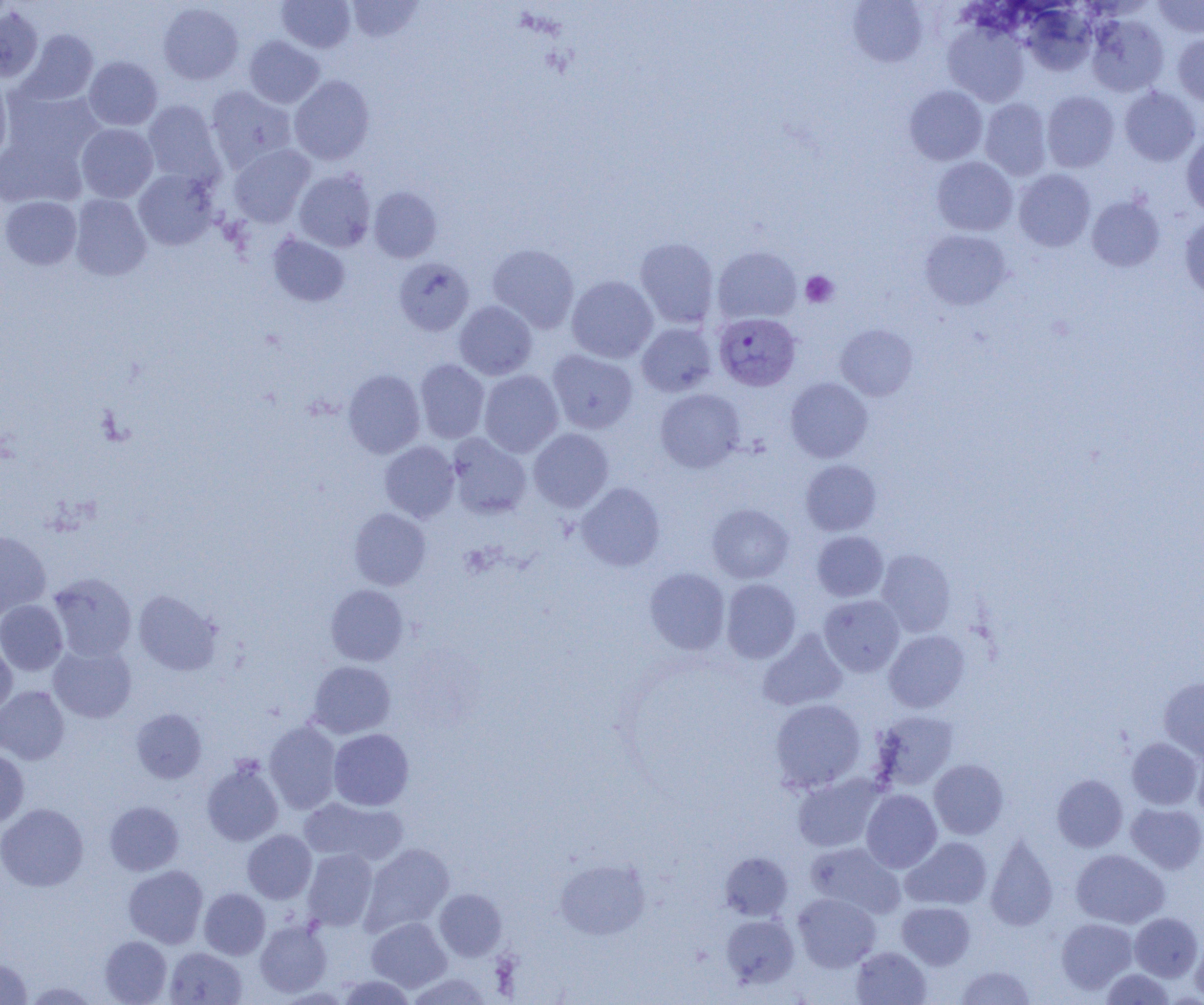
{
  "slide_level_diagnosis": "Plasmodium vivax",
  "modality": "light microscopy",
  "field_of_view": "one of a larger specimen",
  "plasmodium_vivax_infected_red_blood_cell_locations": "approximate bounding boxes as (x1,y1)-(x2,y2) corner pairs in pixels: (714,312)-(801,391)",
  "platelet_locations": "approximate bounding boxes as (x1,y1)-(x2,y2) corner pairs in pixels: (801,271)-(838,308)",
  "magnification": "1000x",
  "uninfected_red_blood_cell_locations": "approximate bounding boxes as (x1,y1)-(x2,y2) corner pairs in pixels: (346,0)-(424,42), (1153,0)-(1204,39), (277,1)-(355,53), (847,1)-(928,67), (158,2)-(244,85), (1021,5)-(1096,75), (0,6)-(44,83), (1087,14)-(1169,97), (942,20)-(1030,107), (18,30)-(99,105), (1173,33)-(1204,106), (244,35)-(324,108), (83,56)-(162,130), (289,75)-(375,165), (0,78)-(12,163), (904,85)-(987,165), (205,86)-(297,172), (1118,87)-(1201,166), (2,88)-(104,171), (1042,90)-(1119,173), (980,98)-(1052,180), (142,100)-(224,186), (76,123)-(158,202), (0,132)-(86,208), (1181,134)-(1204,216), (229,144)-(315,227), (932,156)-(1018,236), (293,168)-(375,252), (133,169)-(217,250), (1013,169)-(1095,252), (369,186)-(442,262), (70,194)-(152,281), (0,195)-(82,270), (1086,195)-(1165,272), (1179,215)-(1204,298), (920,229)-(1012,310), (268,233)-(350,307), (634,237)-(719,328), (487,243)-(579,333), (712,246)-(801,325), (393,257)-(474,335), (566,275)-(658,363), (454,301)-(537,380), (636,322)-(717,397), (836,324)-(917,400), (547,349)-(638,434), (415,359)-(489,443), (342,368)-(425,458), (479,370)-(564,457), (785,377)-(873,463), (655,388)-(745,473), (528,428)-(613,512), (447,433)-(531,518), (380,441)-(459,522), (800,460)-(881,535), (576,482)-(665,571), (707,503)-(794,583), (349,508)-(431,590), (0,529)-(51,620), (812,531)-(888,601), (876,549)-(956,637), (645,567)-(730,654), (48,573)-(137,662), (721,578)-(801,663), (325,584)-(408,665), (133,590)-(222,676), (819,595)-(904,676), (0,600)-(68,676), (758,629)-(847,711), (883,630)-(969,713), (0,639)-(17,718), (48,643)-(136,723), (307,661)-(395,738), (1158,677)-(1204,762), (0,686)-(69,764), (771,698)-(866,792), (131,708)-(207,783), (872,710)-(959,790), (264,721)-(342,814), (328,728)-(414,810), (1126,737)-(1203,810), (1192,744)-(1204,824), (0,748)-(29,827), (202,759)-(284,846), (929,759)-(1009,839), (793,773)-(885,853), (1052,774)-(1128,852), (861,789)-(942,872), (299,797)-(407,866), (105,801)-(184,875), (1126,802)-(1204,874), (0,803)-(88,891), (243,829)-(317,903), (985,834)-(1058,931), (901,836)-(992,910), (804,842)-(905,918), (360,843)-(454,935), (1071,848)-(1169,928), (302,849)-(377,930), (720,851)-(793,920), (554,857)-(651,940), (124,865)-(208,948), (199,888)-(270,959), (434,889)-(507,961), (793,893)-(881,971), (897,901)-(976,969), (1130,912)-(1203,981), (721,914)-(799,989), (367,917)-(451,992), (1056,918)-(1137,994), (255,919)-(332,997), (99,935)-(171,1004), (1190,935)-(1204,1003), (852,946)-(931,1004), (165,947)-(247,1004), (0,958)-(33,1004), (955,965)-(1035,1004), (1101,968)-(1175,1004), (407,973)-(492,1004), (336,975)-(417,1004)",
  "image_size": "1204×1005 pixels",
  "preparation": "thin blood smear"
}